Describe the morphology of the red blood cells.
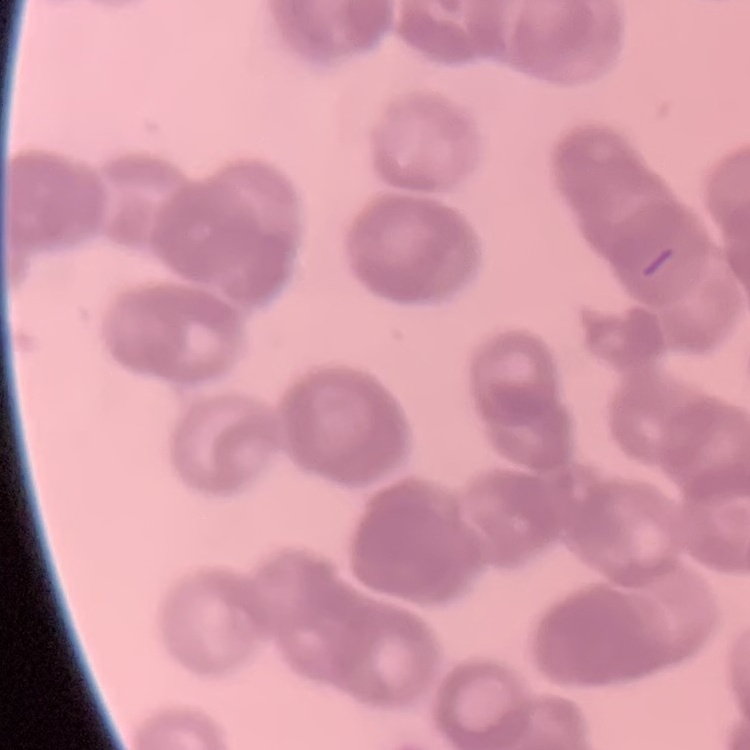

Rouleaux formation.

Thin peripheral smear. One tile cut from a larger photomicrograph. Field's or Giemsa stain.